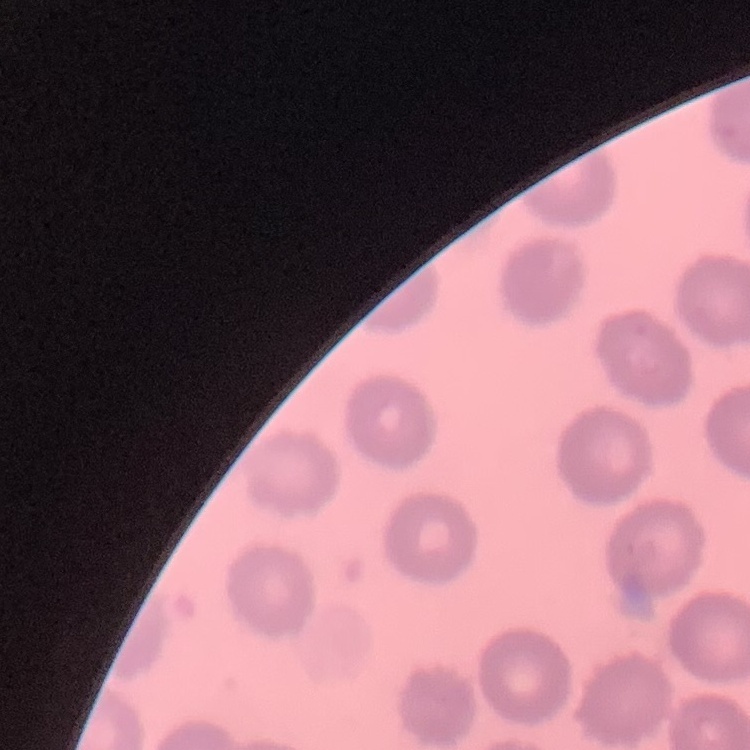

Summary:
  - Red blood cell morphology: no rouleaux formation
  - Image type: square crop of a larger photomicrograph
  - Stain: Field's or Giemsa
  - Preparation: thin blood smear